Evaluate for malaria.
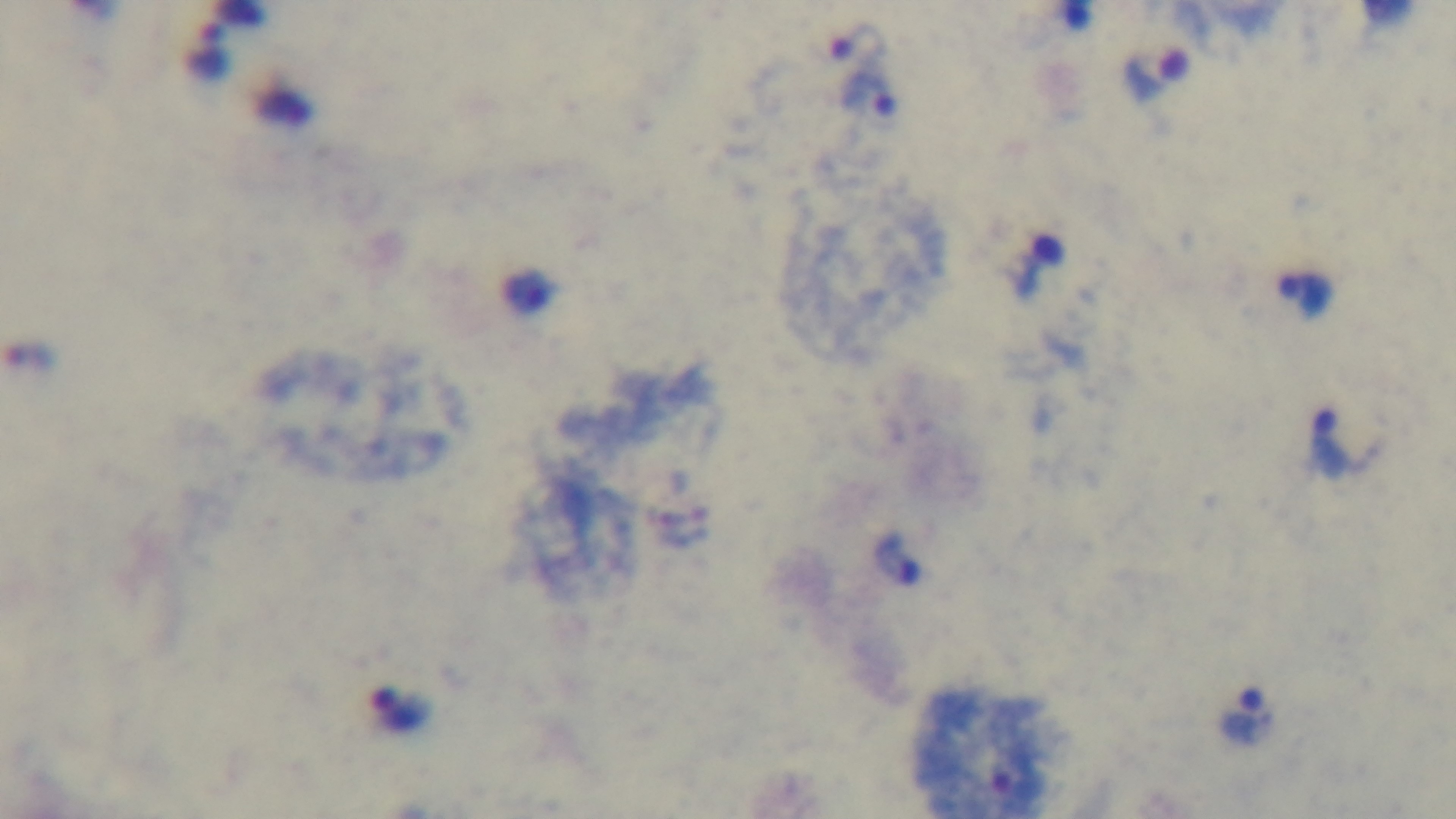

Positive.

Preparation: thick smear. Single field of view. 100x oil-immersion objective. Photomicrograph. Mounted 4K digital camera. Giemsa stain.